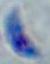

identification: Toxoplasma gondii
magnification: 1000x
modality: micrograph